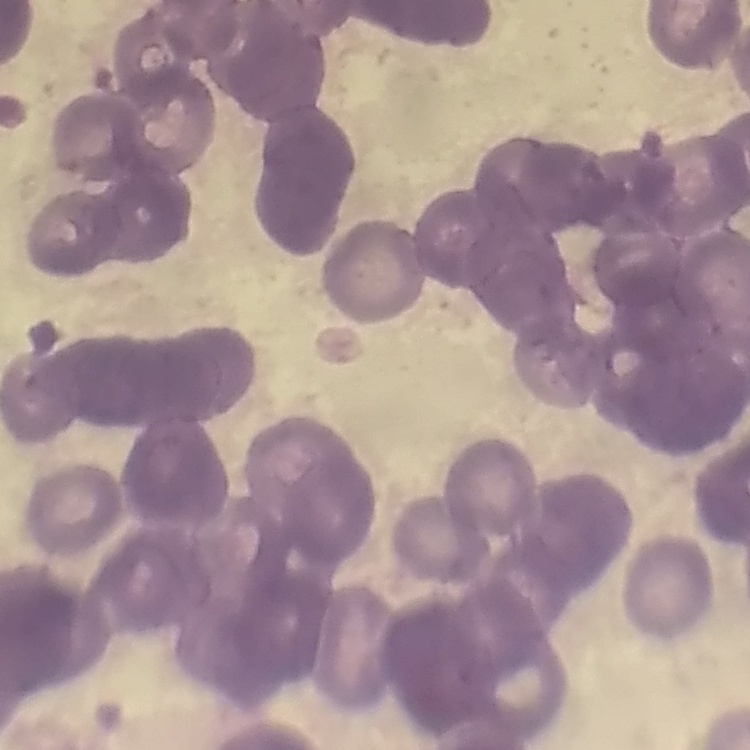

Summary:
  - Erythrocyte morphology: rouleaux formation
  - Image type: square crop of a larger photomicrograph
  - Stain: Field's or Giemsa
  - Preparation: thin blood film